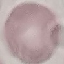
{
  "malaria_status": "uninfected",
  "preparation": "thin blood film",
  "image_type": "cell patch, automatically extracted from a larger field of view and resized to 64 × 64 pixels",
  "stain": "Giemsa",
  "capture": "smartphone through the microscope eyepiece"
}